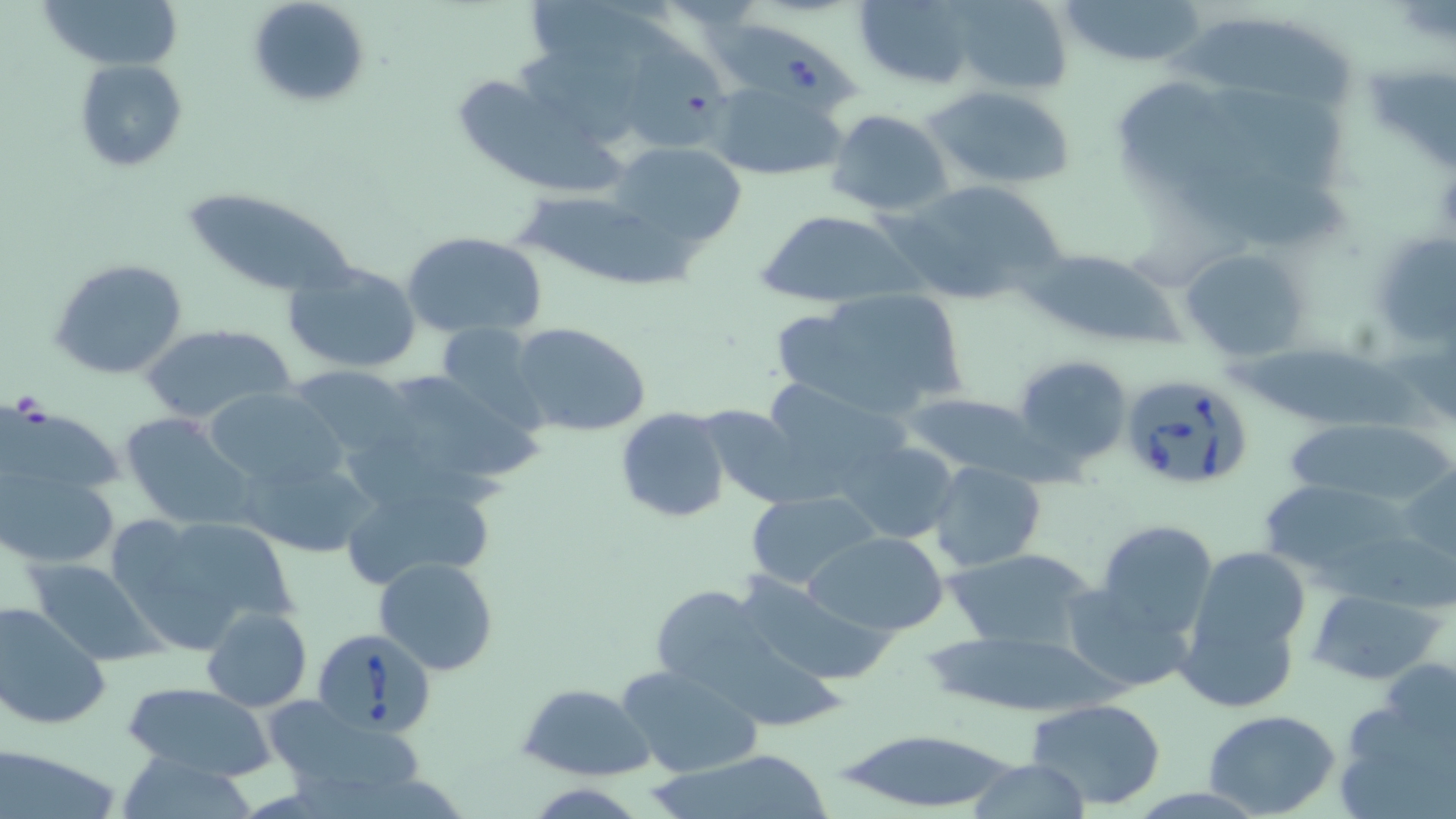

Summary:
  - Coordinate format: approximate bounding boxes as named x1/y1/x2/y2 corners in pixels
  - Babesia divergens-infected red blood cell locations: (x1=704, y1=16, x2=865, y2=115), (x1=1117, y1=372, x2=1254, y2=492), (x1=314, y1=630, x2=437, y2=737)
  - Uninfected red blood cell locations: (x1=36, y1=0, x2=183, y2=70), (x1=248, y1=0, x2=372, y2=111), (x1=953, y1=0, x2=1073, y2=92), (x1=1054, y1=0, x2=1210, y2=68), (x1=853, y1=1, x2=979, y2=89), (x1=1165, y1=16, x2=1361, y2=117), (x1=510, y1=43, x2=649, y2=144), (x1=619, y1=49, x2=742, y2=152), (x1=74, y1=58, x2=188, y2=172), (x1=1115, y1=76, x2=1250, y2=203), (x1=456, y1=81, x2=623, y2=188), (x1=710, y1=82, x2=849, y2=182), (x1=925, y1=85, x2=1076, y2=191), (x1=1207, y1=88, x2=1353, y2=193), (x1=827, y1=109, x2=952, y2=217), (x1=613, y1=141, x2=747, y2=248), (x1=1172, y1=163, x2=1353, y2=251), (x1=887, y1=178, x2=1065, y2=306), (x1=179, y1=185, x2=358, y2=298), (x1=520, y1=201, x2=707, y2=287), (x1=754, y1=210, x2=920, y2=307), (x1=1368, y1=228, x2=1455, y2=353), (x1=401, y1=230, x2=548, y2=339), (x1=1179, y1=246, x2=1311, y2=360), (x1=1025, y1=248, x2=1179, y2=347), (x1=49, y1=256, x2=188, y2=380), (x1=282, y1=260, x2=423, y2=377), (x1=775, y1=285, x2=972, y2=422), (x1=430, y1=322, x2=552, y2=433), (x1=510, y1=322, x2=654, y2=439), (x1=137, y1=323, x2=299, y2=422), (x1=1225, y1=339, x2=1445, y2=435), (x1=1013, y1=353, x2=1134, y2=469), (x1=286, y1=363, x2=416, y2=464), (x1=353, y1=366, x2=537, y2=507), (x1=754, y1=377, x2=915, y2=500), (x1=202, y1=388, x2=346, y2=492), (x1=901, y1=391, x2=1042, y2=480), (x1=1, y1=402, x2=129, y2=488), (x1=695, y1=404, x2=807, y2=508), (x1=615, y1=407, x2=733, y2=524), (x1=120, y1=413, x2=258, y2=530), (x1=1285, y1=417, x2=1452, y2=509), (x1=841, y1=441, x2=962, y2=545), (x1=240, y1=453, x2=377, y2=560), (x1=928, y1=461, x2=1047, y2=573), (x1=1401, y1=463, x2=1456, y2=568), (x1=2, y1=470, x2=119, y2=568), (x1=334, y1=472, x2=496, y2=591), (x1=1258, y1=480, x2=1415, y2=584), (x1=745, y1=490, x2=880, y2=590), (x1=109, y1=512, x2=296, y2=651), (x1=1093, y1=519, x2=1218, y2=642), (x1=805, y1=530, x2=951, y2=635), (x1=944, y1=544, x2=1104, y2=653), (x1=1194, y1=548, x2=1315, y2=651), (x1=27, y1=557, x2=162, y2=666), (x1=374, y1=557, x2=499, y2=675), (x1=734, y1=572, x2=895, y2=687), (x1=1059, y1=579, x2=1193, y2=694), (x1=648, y1=584, x2=774, y2=698), (x1=1306, y1=589, x2=1442, y2=684), (x1=0, y1=598, x2=110, y2=731), (x1=201, y1=607, x2=312, y2=712), (x1=1177, y1=614, x2=1300, y2=713), (x1=924, y1=631, x2=1121, y2=716), (x1=1379, y1=656, x2=1454, y2=748), (x1=615, y1=665, x2=763, y2=780), (x1=124, y1=682, x2=277, y2=781), (x1=519, y1=683, x2=656, y2=781), (x1=1334, y1=690, x2=1456, y2=819), (x1=1026, y1=697, x2=1168, y2=810), (x1=261, y1=698, x2=427, y2=809), (x1=1203, y1=710, x2=1340, y2=817), (x1=832, y1=728, x2=1026, y2=814), (x1=5, y1=740, x2=123, y2=818), (x1=650, y1=744, x2=828, y2=819), (x1=114, y1=756, x2=265, y2=817), (x1=963, y1=758, x2=1096, y2=817)
  - Slide-level diagnosis: Babesia divergens
  - Preparation: thin blood film
  - Magnification: 1000x
  - Image size: 1456×819 pixels
  - Modality: light microscopy
  - Field of view: one of a larger specimen
  - Stain: May-Grünwald-Giemsa